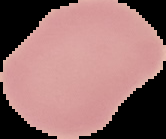 From a thin blood smear. Image is 166×139 pixels. Cell region segmented out of the field of view; the surrounding area is masked to black. Result: no malaria parasites detected.